Report the malaria status of this cell.
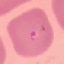

It is parasitized.

Summary:
  - Preparation: thin blood film
  - Image type: cell patch, automatically extracted from a larger field of view and resized to 64 × 64 pixels
  - Capture: smartphone through the microscope eyepiece
  - Stain: Giemsa